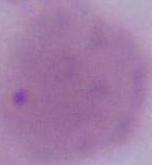

1000x magnification. A red blood cell is seen. Micrograph.